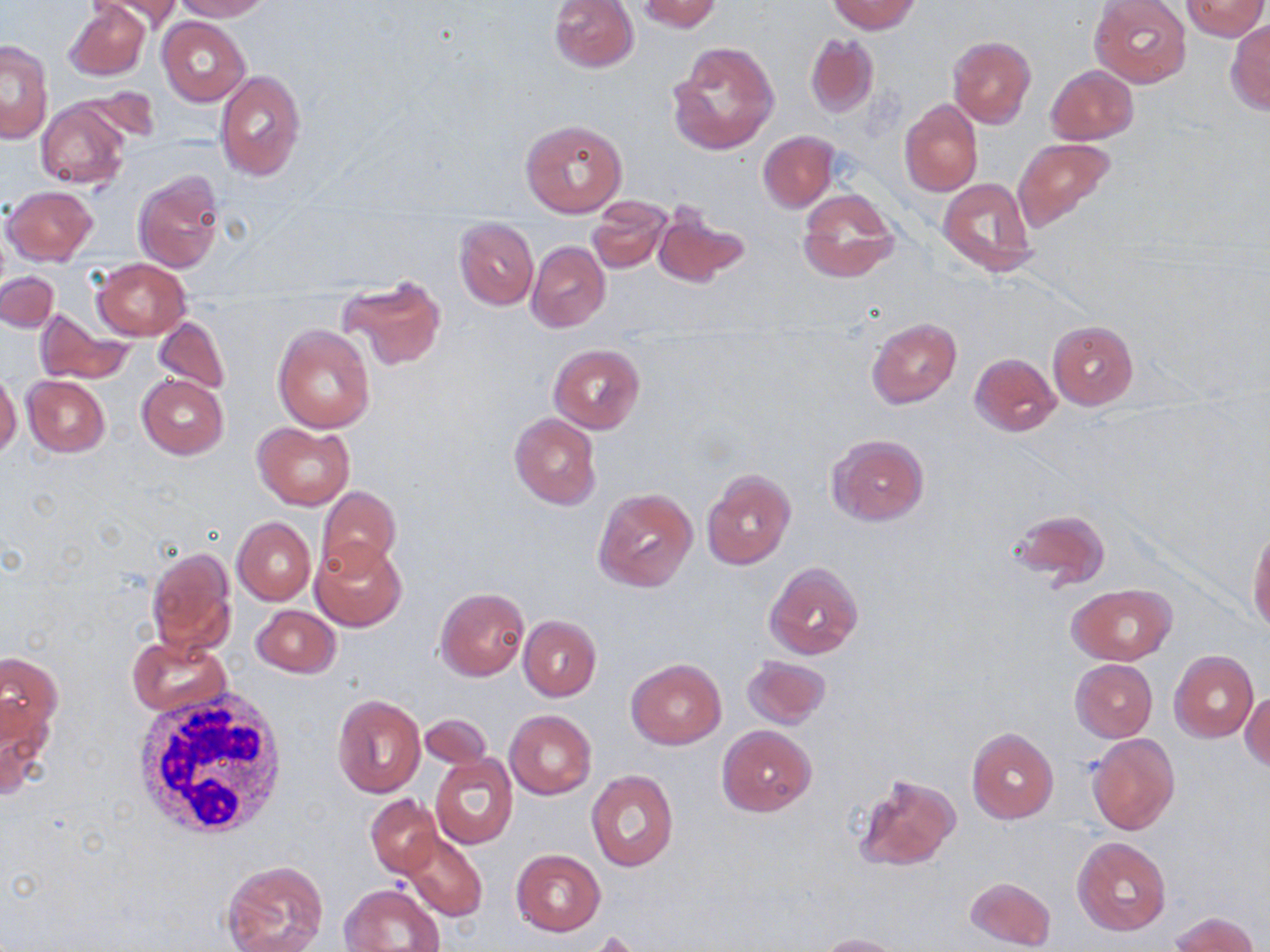

{
  "slide_level_diagnosis": "negative for blood parasites",
  "field_of_view": "one of a larger specimen",
  "stain": "May-Grünwald-Giemsa",
  "modality": "light microscopy",
  "magnification": "1000x",
  "preparation": "thin blood film",
  "white_blood_cell_locations": "approximate bounding boxes as named x1/y1/x2/y2 corners in pixels: (x1=133, y1=686, x2=292, y2=844)",
  "uninfected_red_blood_cell_locations": "approximate bounding boxes as named x1/y1/x2/y2 corners in pixels: (x1=63, y1=0, x2=149, y2=81), (x1=91, y1=0, x2=184, y2=35), (x1=171, y1=0, x2=269, y2=21), (x1=550, y1=0, x2=639, y2=72), (x1=638, y1=0, x2=721, y2=33), (x1=828, y1=0, x2=920, y2=34), (x1=1091, y1=0, x2=1191, y2=86), (x1=1181, y1=0, x2=1268, y2=40), (x1=156, y1=17, x2=250, y2=105), (x1=1227, y1=19, x2=1270, y2=113), (x1=805, y1=34, x2=880, y2=118), (x1=947, y1=36, x2=1036, y2=128), (x1=1, y1=40, x2=52, y2=142), (x1=668, y1=41, x2=779, y2=155), (x1=1046, y1=65, x2=1138, y2=144), (x1=215, y1=69, x2=306, y2=181), (x1=72, y1=86, x2=161, y2=145), (x1=900, y1=99, x2=983, y2=196), (x1=36, y1=100, x2=128, y2=189), (x1=520, y1=118, x2=627, y2=217), (x1=758, y1=130, x2=838, y2=211), (x1=1014, y1=137, x2=1115, y2=229), (x1=132, y1=171, x2=223, y2=272), (x1=937, y1=176, x2=1039, y2=277), (x1=3, y1=185, x2=97, y2=264), (x1=796, y1=188, x2=899, y2=283), (x1=588, y1=197, x2=671, y2=273), (x1=652, y1=203, x2=748, y2=289), (x1=455, y1=218, x2=538, y2=310), (x1=527, y1=242, x2=611, y2=332), (x1=92, y1=257, x2=190, y2=340), (x1=1, y1=272, x2=58, y2=333), (x1=337, y1=274, x2=446, y2=370), (x1=34, y1=309, x2=132, y2=385), (x1=153, y1=315, x2=230, y2=396), (x1=866, y1=317, x2=962, y2=408), (x1=1047, y1=320, x2=1138, y2=409), (x1=273, y1=323, x2=375, y2=432), (x1=548, y1=342, x2=646, y2=435), (x1=970, y1=352, x2=1061, y2=437), (x1=0, y1=371, x2=21, y2=459), (x1=137, y1=374, x2=229, y2=458), (x1=22, y1=375, x2=109, y2=458), (x1=510, y1=413, x2=601, y2=509), (x1=253, y1=422, x2=355, y2=510), (x1=828, y1=434, x2=930, y2=526), (x1=702, y1=468, x2=795, y2=570), (x1=316, y1=486, x2=400, y2=581), (x1=592, y1=487, x2=698, y2=593), (x1=1007, y1=510, x2=1110, y2=590), (x1=233, y1=516, x2=314, y2=604), (x1=1247, y1=524, x2=1269, y2=634), (x1=310, y1=540, x2=407, y2=630), (x1=145, y1=547, x2=234, y2=656), (x1=763, y1=561, x2=865, y2=661), (x1=1068, y1=584, x2=1174, y2=665), (x1=435, y1=588, x2=528, y2=680), (x1=250, y1=605, x2=341, y2=678), (x1=518, y1=616, x2=601, y2=701), (x1=127, y1=638, x2=231, y2=716), (x1=1170, y1=651, x2=1258, y2=741), (x1=0, y1=652, x2=62, y2=748), (x1=741, y1=655, x2=832, y2=729), (x1=625, y1=657, x2=727, y2=749), (x1=1070, y1=659, x2=1157, y2=743), (x1=1241, y1=689, x2=1269, y2=772), (x1=333, y1=694, x2=425, y2=798), (x1=1, y1=702, x2=53, y2=802), (x1=504, y1=709, x2=595, y2=799), (x1=419, y1=715, x2=491, y2=769), (x1=717, y1=724, x2=818, y2=818), (x1=966, y1=727, x2=1059, y2=823), (x1=1087, y1=732, x2=1181, y2=835), (x1=429, y1=753, x2=517, y2=849), (x1=586, y1=770, x2=679, y2=871), (x1=851, y1=773, x2=961, y2=872), (x1=365, y1=795, x2=442, y2=879), (x1=401, y1=831, x2=487, y2=922), (x1=1073, y1=836, x2=1170, y2=934), (x1=511, y1=849, x2=605, y2=936), (x1=223, y1=860, x2=329, y2=952), (x1=963, y1=876, x2=1057, y2=951), (x1=339, y1=884, x2=443, y2=951), (x1=1171, y1=912, x2=1259, y2=952), (x1=817, y1=933, x2=905, y2=952)",
  "image_size": "1270×952 pixels"
}